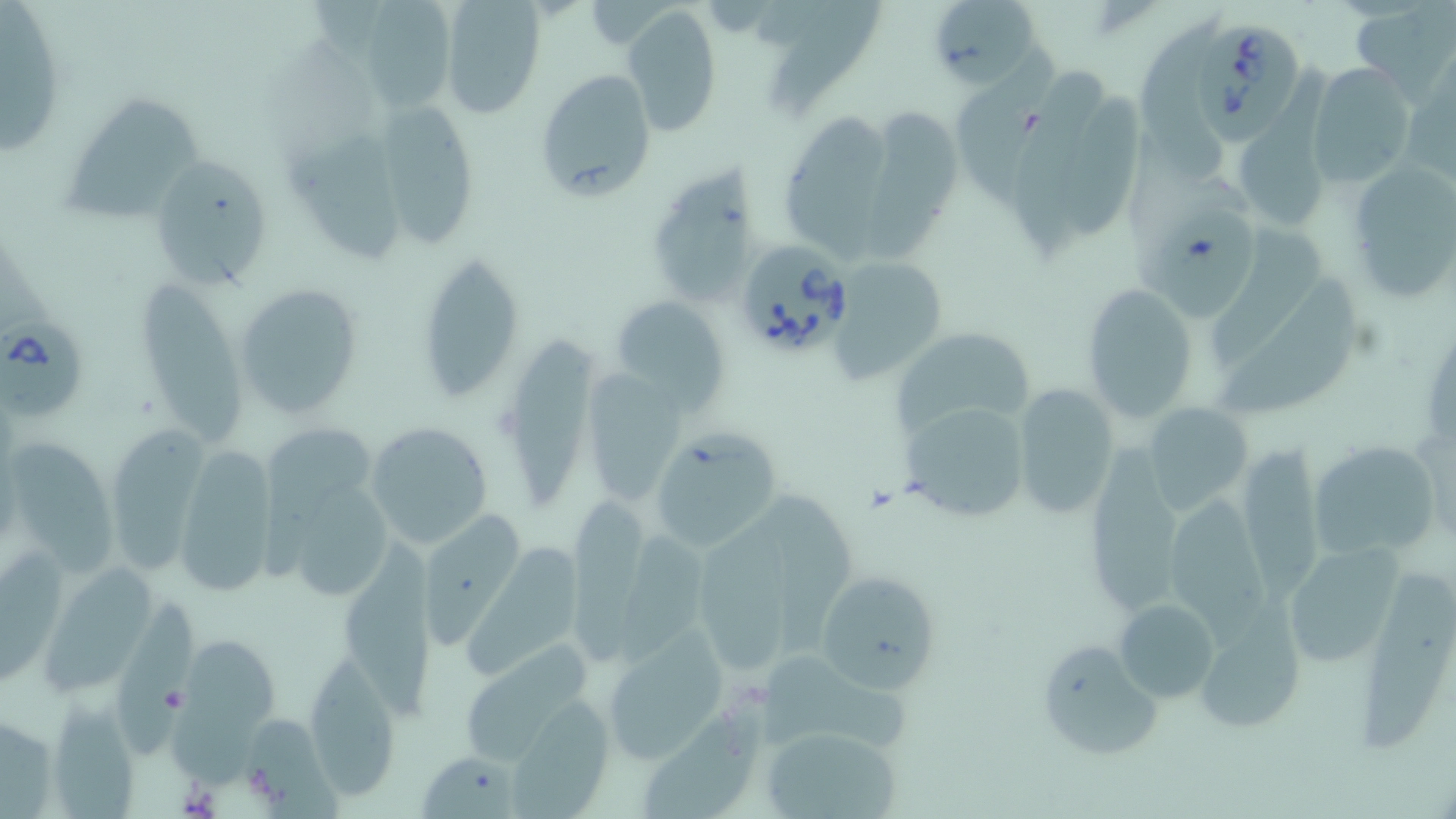 Approximate bounding boxes as [x1, y1, x2, y2] in pixels. Babesia divergens-infected red blood cell locations: [1195, 19, 1307, 135], [733, 239, 854, 358], [0, 313, 86, 424]. Platelet locations: [1089, 3, 1152, 41], [159, 684, 189, 713]. Uninfected red blood cell locations: [365, 0, 457, 114], [438, 0, 545, 116], [767, 0, 877, 114], [927, 0, 1046, 91], [1351, 1, 1456, 99], [1, 3, 67, 159], [622, 5, 723, 135], [1144, 9, 1245, 185], [953, 48, 1056, 230], [1015, 62, 1107, 260], [1307, 62, 1417, 189], [534, 67, 660, 200], [60, 94, 211, 219], [1067, 94, 1147, 235], [378, 99, 479, 248], [866, 103, 961, 267], [784, 114, 895, 263], [1231, 120, 1330, 232], [290, 124, 406, 267], [148, 157, 270, 289], [1344, 158, 1456, 305], [649, 161, 767, 296], [1133, 180, 1264, 322], [1207, 225, 1332, 355], [417, 251, 524, 400], [828, 254, 949, 381], [1219, 271, 1365, 418], [141, 277, 242, 450], [233, 279, 367, 420], [1082, 283, 1199, 424], [610, 295, 731, 410], [891, 326, 1038, 440], [506, 333, 603, 510], [581, 371, 686, 506], [1011, 385, 1120, 520], [899, 398, 1033, 523], [1141, 404, 1251, 515], [365, 421, 493, 551], [266, 422, 374, 578], [110, 425, 213, 577], [651, 430, 778, 550], [1308, 432, 1438, 562], [1093, 437, 1186, 614], [12, 443, 121, 580], [1236, 446, 1325, 601], [175, 449, 278, 596], [1164, 485, 1278, 649], [300, 487, 395, 601], [767, 488, 862, 657], [568, 501, 648, 666], [698, 505, 806, 680], [416, 510, 526, 644], [623, 526, 713, 665], [463, 544, 581, 687], [1285, 544, 1402, 669], [346, 545, 435, 722], [2, 549, 70, 689], [46, 561, 158, 696], [1360, 563, 1449, 756], [813, 569, 942, 694], [122, 597, 201, 757], [1114, 599, 1221, 702], [1194, 612, 1307, 736], [600, 628, 732, 764], [180, 637, 279, 791], [1034, 637, 1164, 763], [456, 641, 598, 771], [761, 646, 920, 756], [314, 655, 397, 800], [642, 686, 757, 819], [48, 697, 137, 819], [507, 701, 612, 817], [0, 713, 60, 815], [243, 717, 340, 819], [756, 723, 906, 819], [422, 757, 521, 819]. Slide-level diagnosis: Babesia divergens. Light microscopy. One field of a larger specimen. May-Grünwald-Giemsa stain. Thin blood smear. Image is 1456×819 pixels. Captured at 1000x magnification.